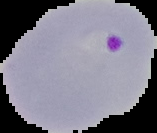
Image is 157×133 pixels. Result: malaria parasites identified. From a thin blood film. Segmented cell region on a black background.